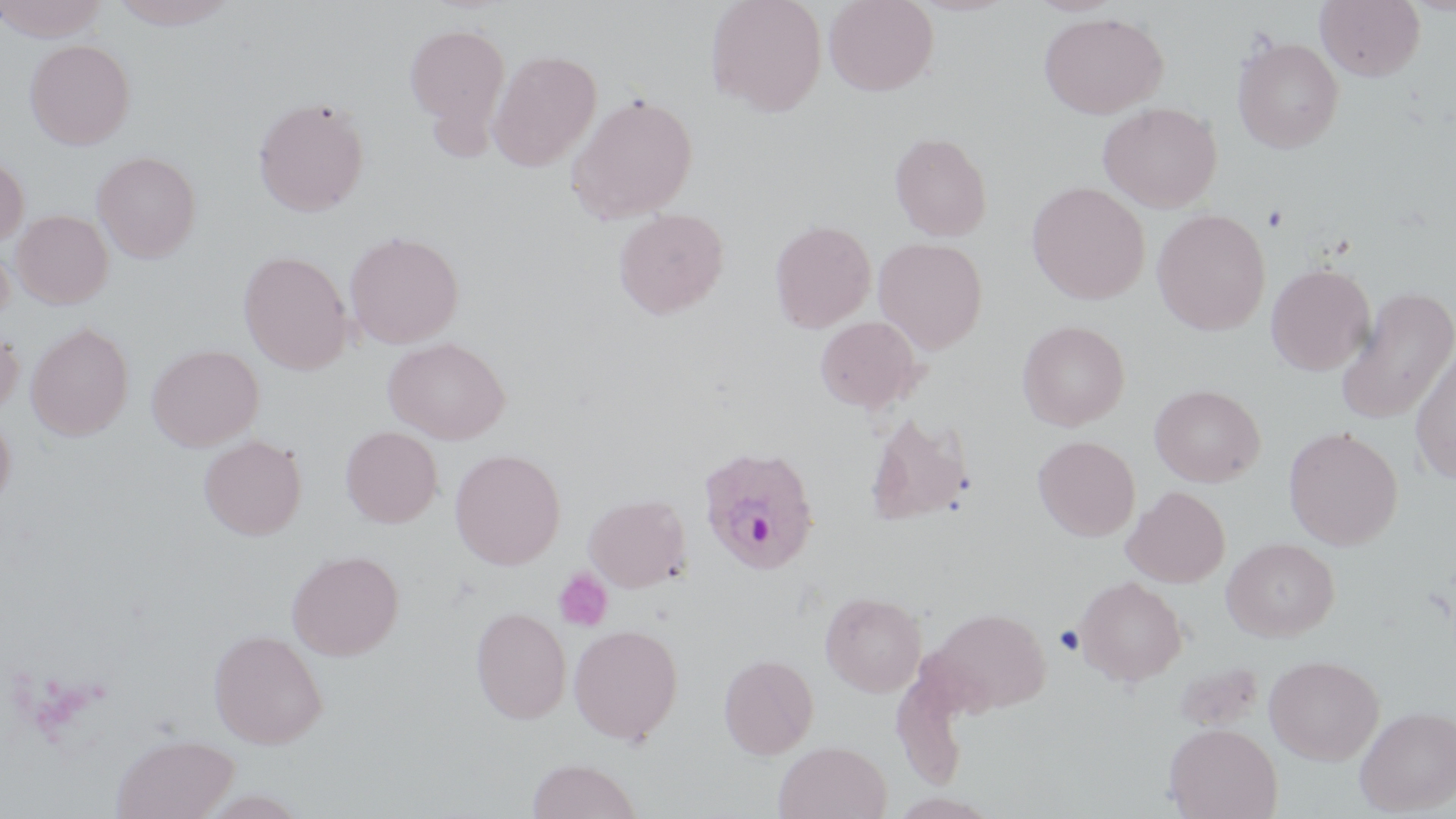 Approximate bounding boxes as (x1, y1, x2, y2) in pixels. Plasmodium ovale-infected red blood cell locations: (697, 444, 820, 574). Uninfected red blood cell locations: (0, 0, 111, 41), (109, 0, 239, 29), (705, 0, 826, 116), (823, 0, 939, 95), (1315, 0, 1425, 81), (1039, 11, 1167, 119), (404, 22, 511, 138), (1233, 37, 1344, 153), (25, 39, 134, 149), (488, 49, 601, 171), (567, 93, 699, 224), (252, 95, 370, 217), (1098, 102, 1222, 213), (889, 132, 992, 241), (92, 151, 201, 262), (0, 154, 29, 248), (1027, 181, 1149, 304), (612, 208, 729, 319), (11, 209, 113, 308), (1152, 209, 1270, 335), (769, 219, 876, 332), (344, 230, 464, 349), (0, 237, 14, 325), (874, 237, 988, 353), (239, 251, 353, 375), (1265, 262, 1376, 375), (1334, 286, 1456, 426), (814, 316, 925, 413), (1017, 320, 1129, 431), (26, 322, 133, 440), (0, 327, 23, 418), (383, 337, 509, 444), (1409, 342, 1456, 484), (147, 344, 264, 450), (1149, 384, 1266, 487), (0, 411, 16, 508), (864, 412, 973, 525), (340, 426, 442, 527), (1283, 426, 1403, 550), (198, 435, 307, 539), (1033, 435, 1140, 541), (449, 449, 565, 569), (1122, 486, 1231, 588), (584, 493, 690, 592), (1222, 537, 1339, 642), (286, 550, 404, 660), (1074, 576, 1188, 685), (820, 591, 926, 696), (929, 606, 1050, 713), (471, 607, 571, 723), (568, 624, 683, 744), (208, 629, 327, 748), (719, 653, 819, 759), (1264, 654, 1384, 765), (1172, 660, 1264, 732), (891, 661, 970, 792), (1355, 705, 1456, 815), (1164, 723, 1283, 819), (111, 733, 238, 819), (773, 741, 891, 819), (526, 757, 642, 819). Platelet locations: (1262, 204, 1289, 232), (554, 569, 614, 632), (1055, 624, 1084, 656). Slide-level diagnosis: Plasmodium ovale. 1000x magnification. May-Grünwald-Giemsa stain. Optical microscopy. Image is 1456×819 pixels. Single field of view. Thin blood film.